Give the preparation type.
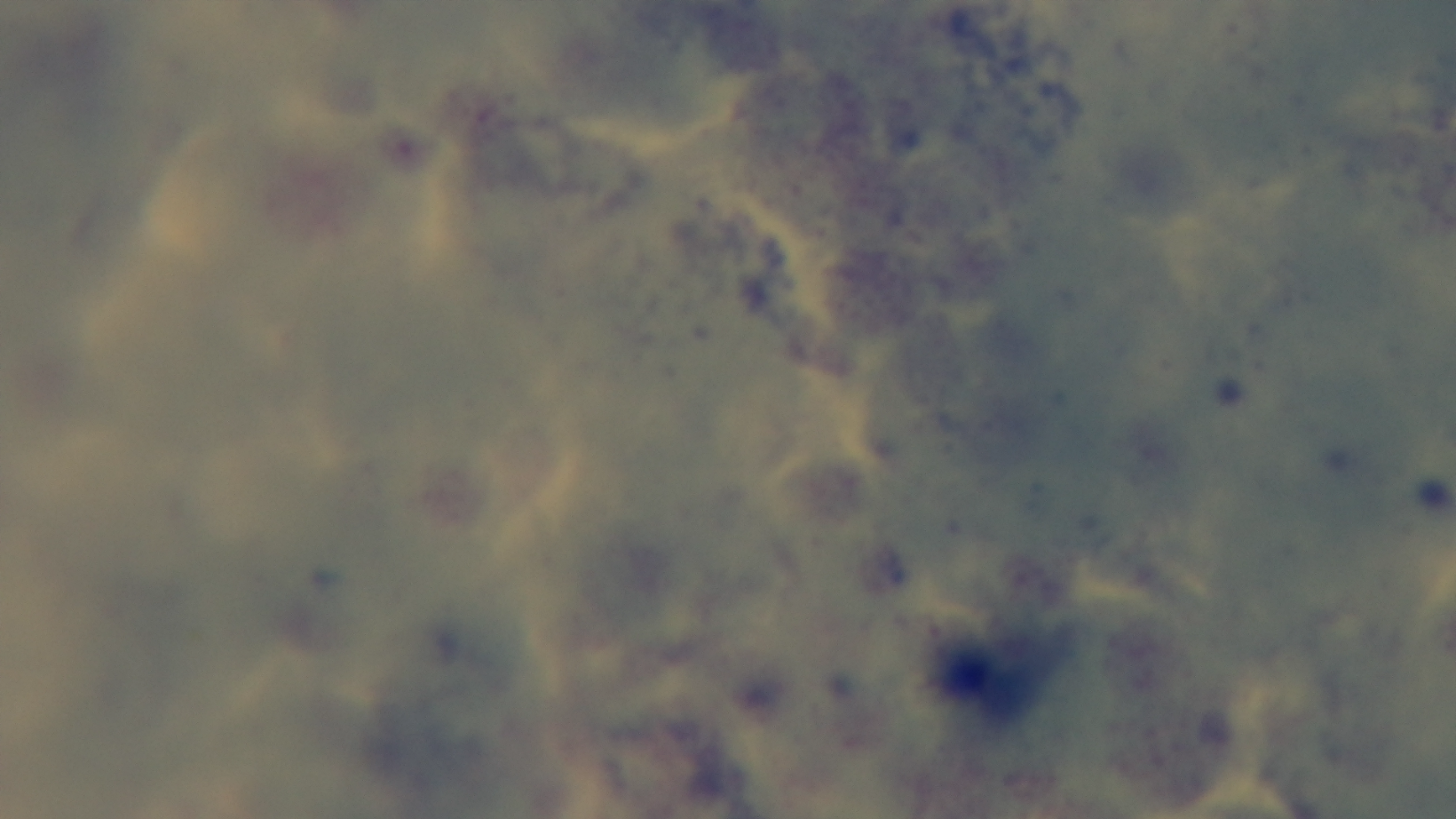
A thick smear.

Summary:
  - Capture: mounted 4K digital camera
  - Field of view: one from the slide
  - Malaria status: negative
  - Stain: Giemsa
  - Objective: 100x oil immersion
  - Modality: light microscopy